Give the extent of all Babesia divergens-infected red blood cells.
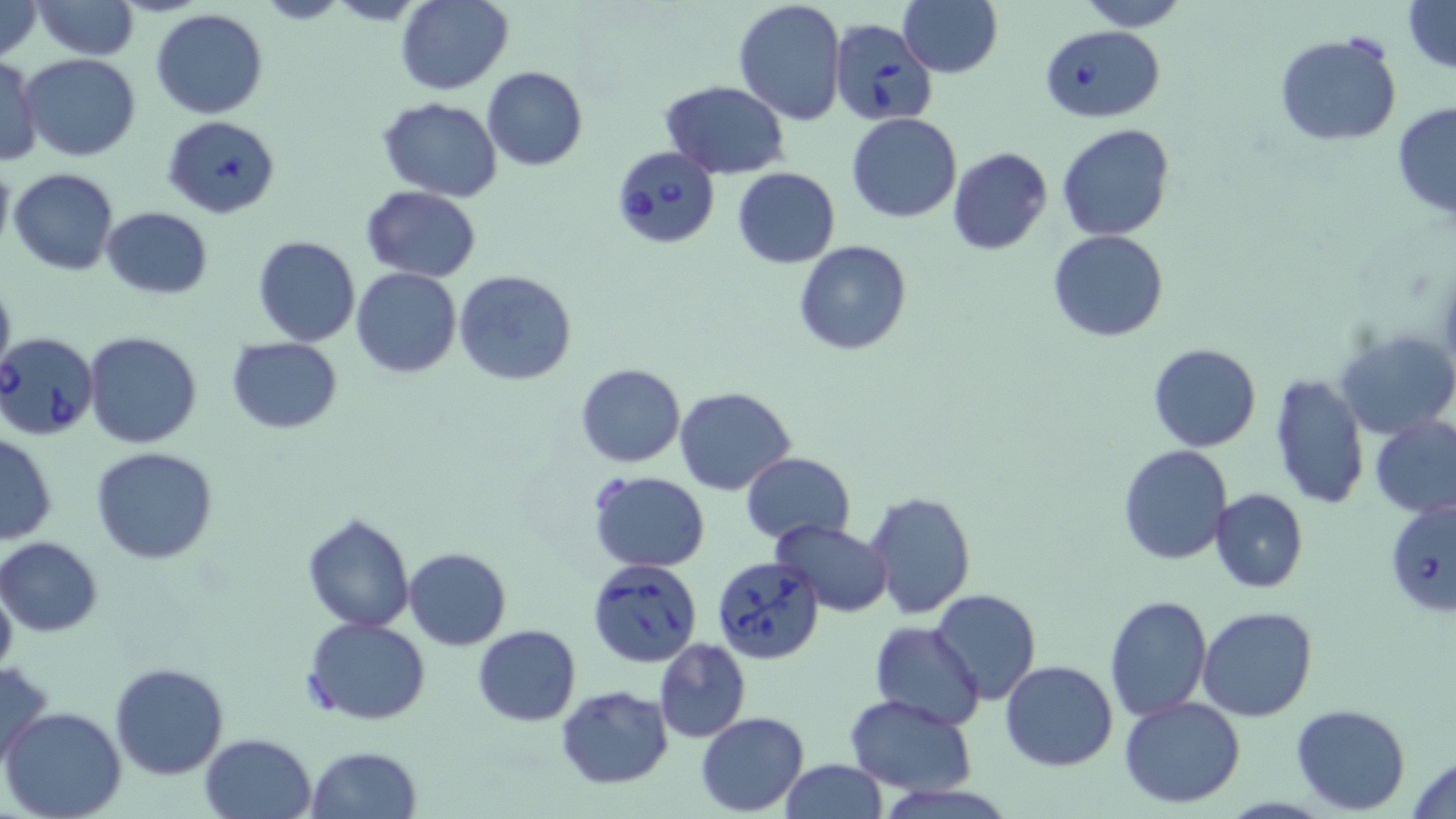
Approximate bounding boxes as (x1,y1)-(x2,y2) corner pairs in pixels.
Babesia divergens-infected red blood cells: (830,20)-(935,126), (1040,25)-(1164,122), (610,147)-(721,249), (0,331)-(103,442), (1386,501)-(1456,618), (707,555)-(827,668), (587,557)-(702,667).

Uninfected red blood cell locations: (0,0)-(42,62), (31,0)-(139,60), (394,0)-(513,93), (732,0)-(847,126), (1075,0)-(1191,30), (1403,0)-(1456,72), (898,1)-(1003,78), (151,9)-(269,119), (1274,32)-(1402,146), (21,52)-(142,161), (0,55)-(43,167), (482,66)-(587,171), (659,81)-(790,180), (377,97)-(503,200), (1392,103)-(1456,222), (846,113)-(962,223), (161,114)-(282,219), (1056,123)-(1175,240), (946,147)-(1054,256), (0,159)-(14,259), (731,167)-(840,267), (8,168)-(119,276), (361,186)-(483,281), (101,206)-(213,299), (1048,231)-(1170,343), (252,235)-(360,347), (793,241)-(912,354), (352,269)-(461,378), (453,270)-(577,387), (0,275)-(16,382), (1335,328)-(1456,440), (82,331)-(201,448), (226,337)-(342,434), (1149,343)-(1261,452), (576,363)-(686,468), (1270,372)-(1370,511), (675,386)-(797,495), (1368,417)-(1456,517), (0,432)-(56,545), (1118,445)-(1233,565), (91,447)-(220,565), (741,452)-(854,545), (588,470)-(710,572), (1210,488)-(1308,594), (864,490)-(976,619), (302,512)-(414,631), (770,518)-(894,617), (0,537)-(102,636), (404,547)-(512,649), (0,578)-(17,680), (930,589)-(1041,706), (1104,595)-(1212,721), (1197,606)-(1317,722), (303,616)-(431,725), (870,621)-(986,731), (472,624)-(582,726), (653,638)-(752,742), (0,658)-(54,771), (999,660)-(1119,770), (109,662)-(229,780), (555,685)-(673,788), (845,694)-(978,796), (1119,695)-(1247,807), (1291,704)-(1410,814), (2,705)-(128,819), (695,712)-(809,816), (199,732)-(317,819), (306,747)-(422,819), (1408,754)-(1456,818), (778,759)-(887,819). Slide-level diagnosis: Babesia divergens. Optical microscopy. Image is 1456×819 pixels. One field of a larger specimen. Thin blood film. May-Grünwald-Giemsa stain. 1000x magnification.